Point out each malaria parasite.
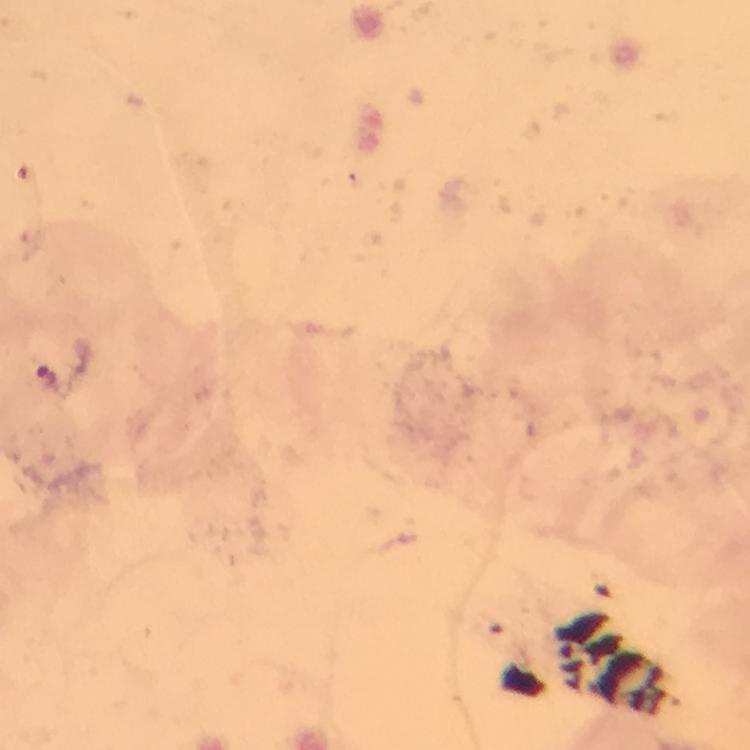

Approximate centers as [x, y] in pixels.
Malaria parasites: [50, 379].

Smartphone photograph taken through a microscope. Image is 750×750 pixels. Giemsa-stained preparation. Thick smear. Cropped region of a single field of view. 100x magnification. From a diagnostic examination for malaria. Immersion oil was used.